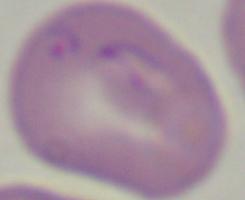
{
  "modality": "micrograph",
  "magnification": "1000x",
  "identification": "Babesia"
}